Identify the parasite.
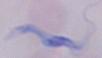

This is a trypanosome.

magnification = 1000x
modality = photomicrograph